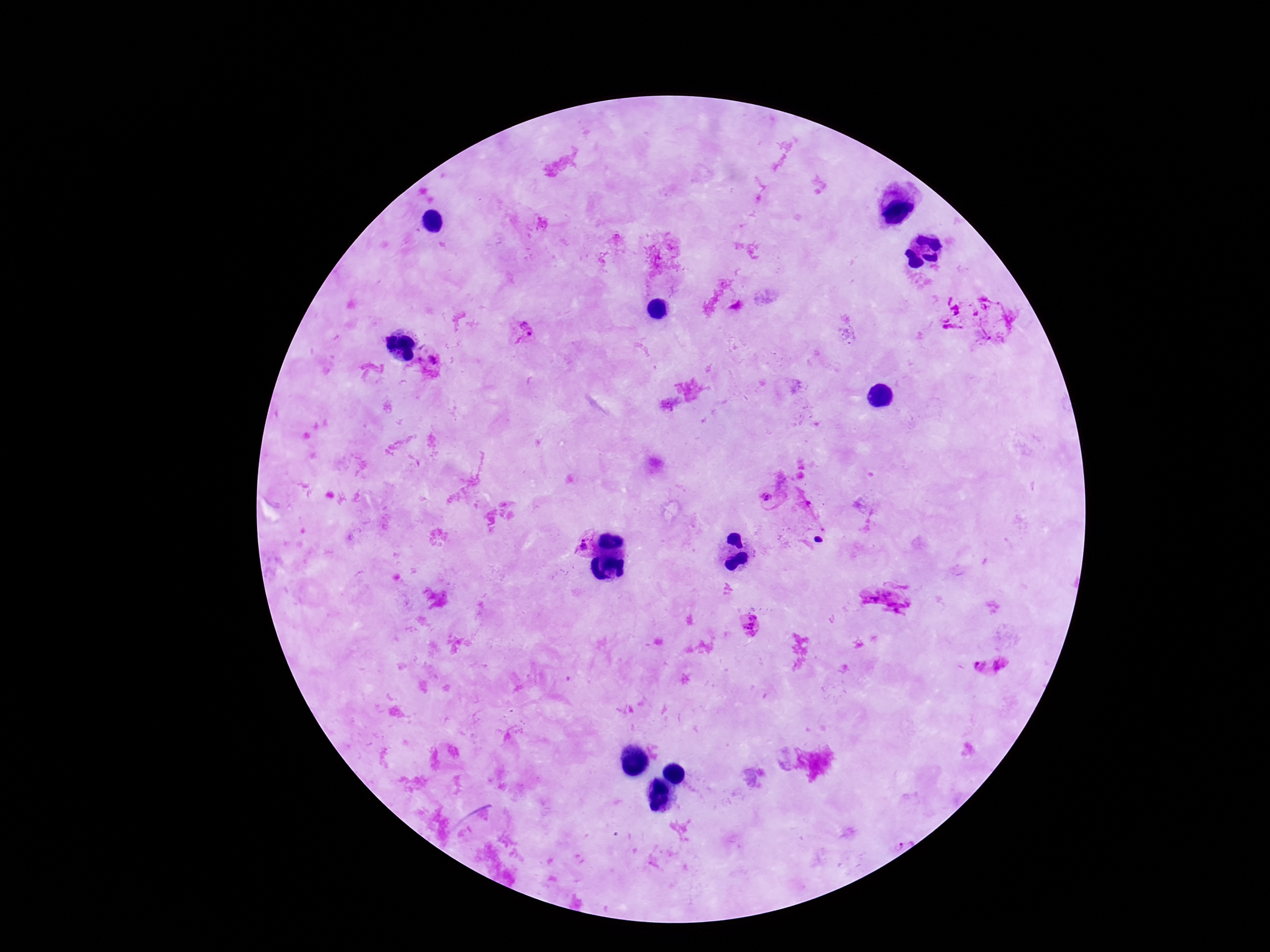
Approximate centers as [x, y] in pixels.
Summary:
  - Plasmodium parasite locations: [526, 330], [433, 361], [766, 496], [584, 544], [749, 626], [991, 669]
  - Stain: Giemsa
  - Capture: smartphone camera through the microscope eyepiece
  - Patient malaria status: positive
  - Preparation: thick peripheral-blood smear
  - Field of view: single
  - Magnification: 100x
  - Image size: 1270×952 pixels